Draw a bounding box around every Plasmodium parasite, every leukocyte, and every artifact (stain precipitate or debris).
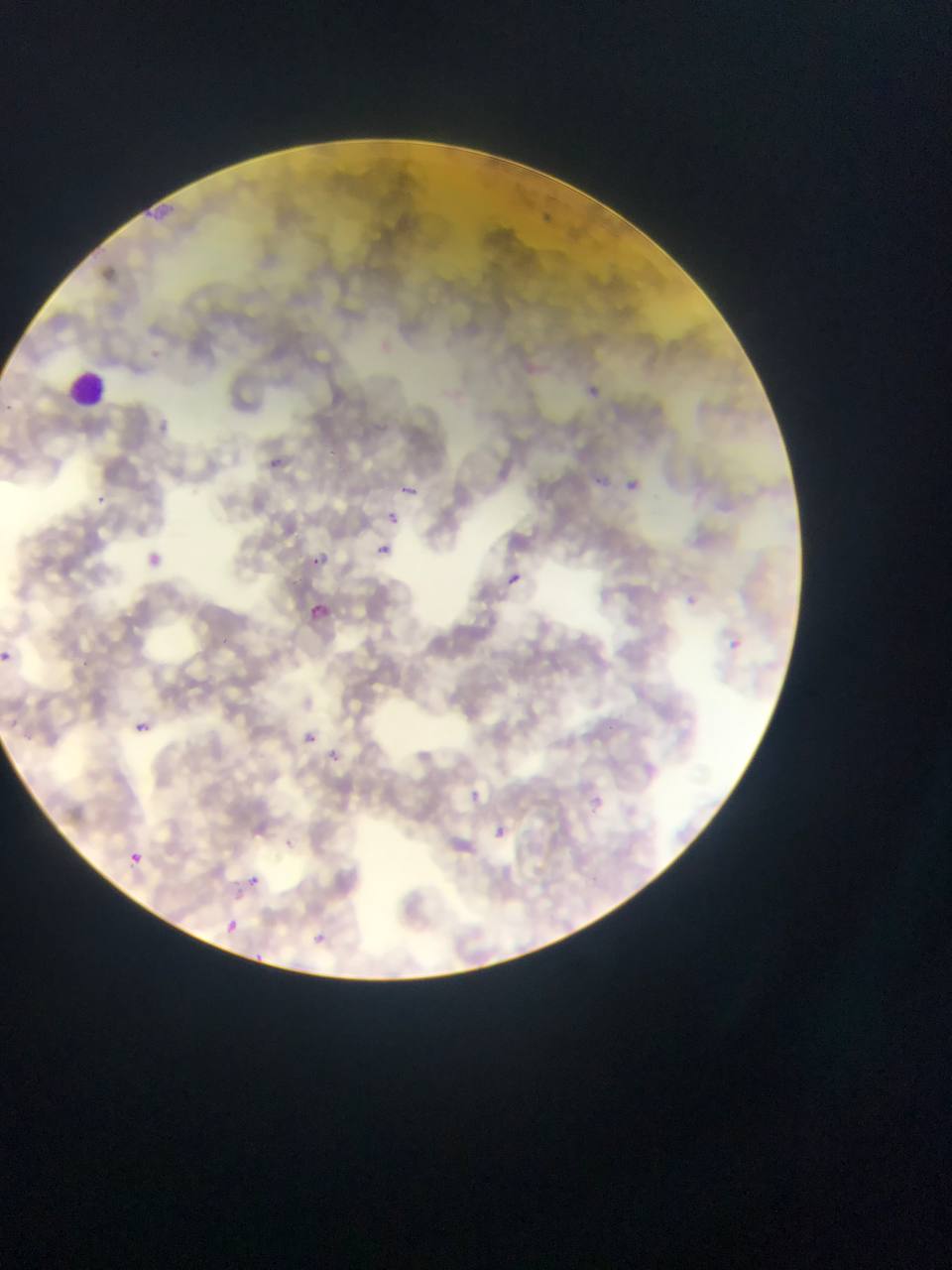
Approximate bounding boxes as left top right bottom in pixels.
Plasmodium parasites: 591 384 608 397; 4 401 17 413; 272 457 292 467; 595 471 612 488; 627 475 644 498; 400 486 428 496; 91 493 113 510; 384 511 407 528; 377 541 392 555; 312 549 336 566; 144 551 161 566; 506 570 526 588; 684 588 697 608; 310 602 332 619; 729 637 741 649; 0 650 11 661; 135 722 151 733; 304 729 326 746; 330 747 340 764; 468 784 489 809; 591 796 606 814; 492 822 510 843; 130 852 144 865; 245 875 266 887; 223 917 243 938; 313 930 329 945; 249 949 263 962.
Leukocytes: 68 371 109 411.

country = Ghana
field of view = single
image size = 952×1270 pixels
capture = mobile-phone photograph through a microscope
preparation = thin blood smear